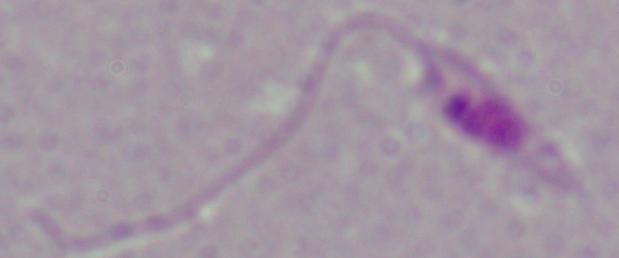 Photomicrograph. A Leishmania parasite is seen. 1000x magnification.